Report the malaria status of this cell.
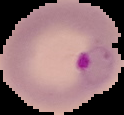

Parasitized.

Summary:
  - Image size: 124×115 pixels
  - Preparation: thin blood film
  - Image type: segmented cell region on a black background